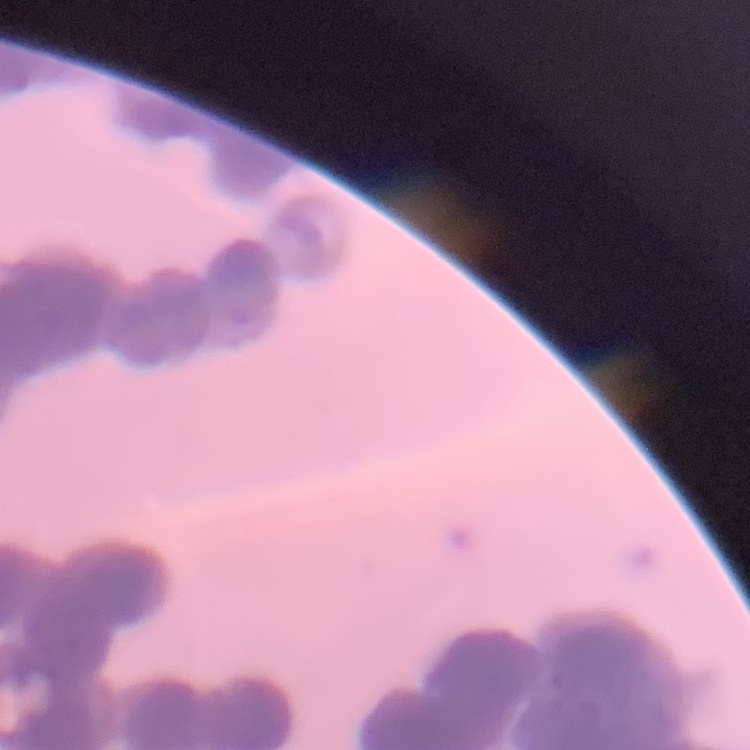
The erythrocytes exhibit rouleaux formation. One tile cut from a larger photomicrograph. Stained with either Field's or Giemsa. Thin blood film.